Evaluate for malaria.
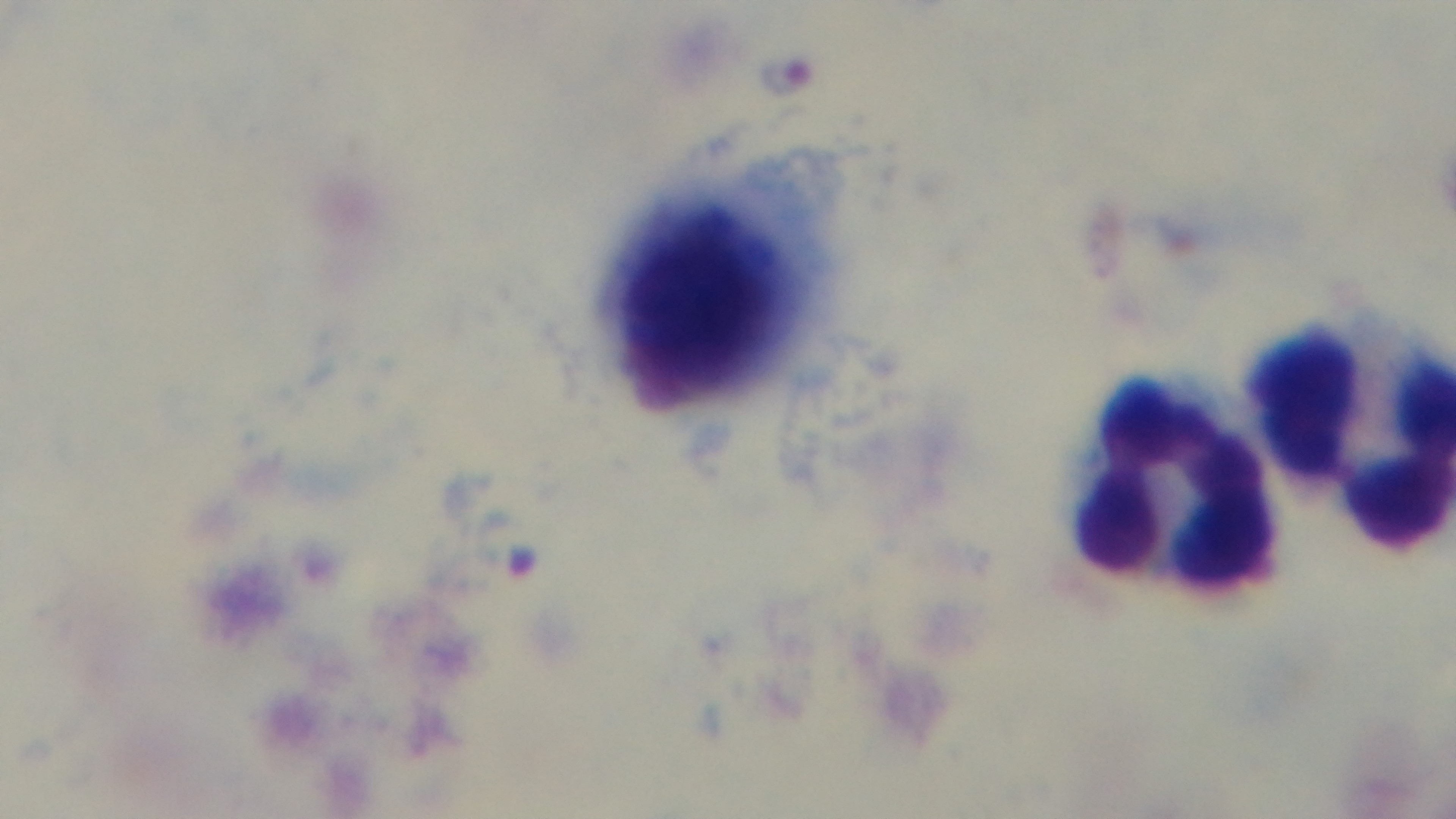

It is infected.

Summary:
  - Modality: light microscopy
  - Capture: mounted 4K digital camera
  - Objective: 100x oil immersion
  - Preparation: thick blood film
  - Field of view: one from the slide
  - Stain: Giemsa